Identify the parasite.
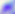
This is Toxoplasma gondii.

Photomicrograph. 400x magnification.